Draw a bounding box around every parasitised red blood cell.
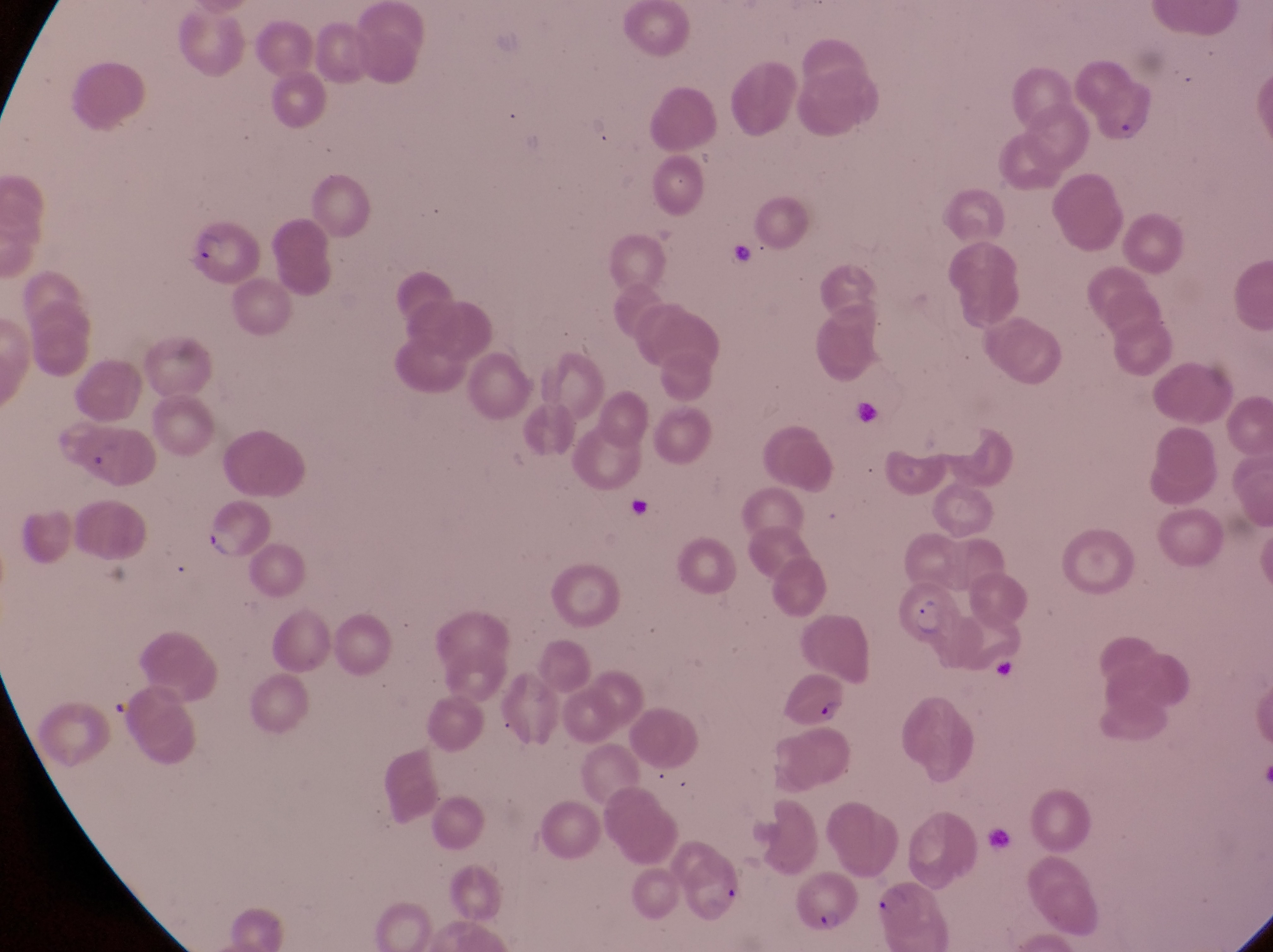
Approximate bounding boxes as (left, top, right, bottom) in pixels.
Parasitised red blood cells: (183, 218, 260, 283), (80, 427, 158, 492), (194, 500, 269, 558), (894, 580, 959, 647), (781, 670, 851, 732), (680, 849, 749, 922), (792, 871, 859, 938), (871, 881, 948, 948).

Summary:
  - Artifact (platelet-like body, stain precipitate, or debris) locations: (844, 397, 879, 424), (622, 489, 655, 528), (991, 656, 1024, 688)
  - Country: Uganda
  - Capture: smartphone photograph through the eyepiece of an Olympus CX-23 microscope
  - Field of view: single
  - Preparation: thin blood film
  - Magnification: 1000x
  - Image size: 1273×952 pixels